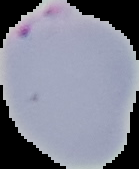
Summary:
  - Malaria status: parasitized
  - Image size: 139×169 pixels
  - Image type: cell region segmented out of the field of view; surrounding area masked to black
  - Preparation: thin blood smear